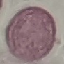

Summary:
  - Result: no malaria parasites seen
  - Stain: Giemsa
  - Capture: smartphone through the microscope eyepiece
  - Preparation: thin smear
  - Image type: automatically extracted cell patch, resized to 64 × 64 pixels